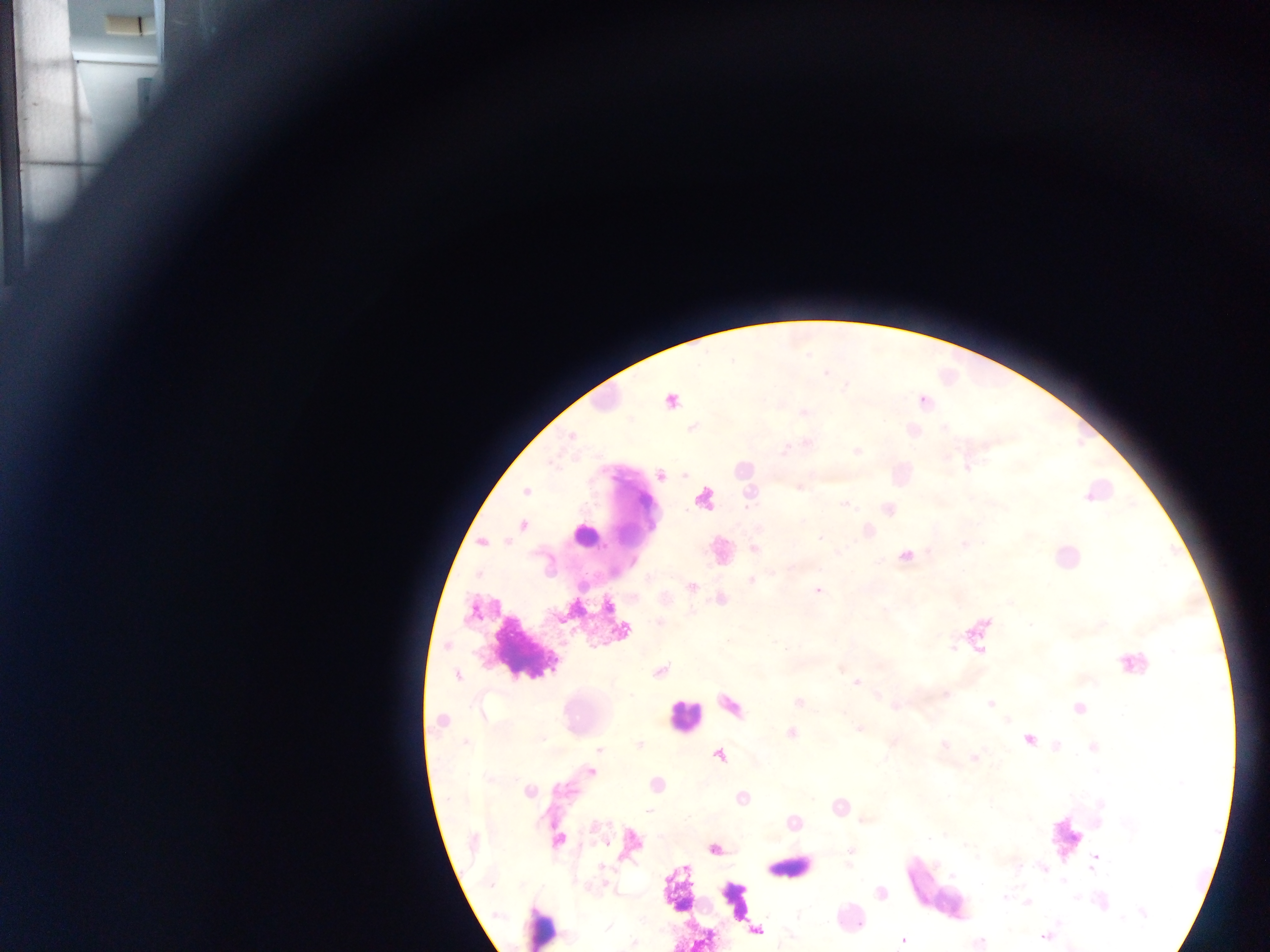 Approximate centers as {x, y} in pixels. Leukocyte locations: {584, 536}, {526, 649}, {1132, 663}, {684, 717}, {1067, 838}, {790, 868}, {676, 890}, {936, 890}, {736, 900}, {540, 926}. Malaria parasite locations: {670, 400}, {922, 401}, {912, 431}, {570, 436}, {856, 451}, {966, 466}, {660, 475}, {798, 485}, {525, 491}, {703, 499}, {844, 503}, {887, 508}, {522, 525}, {482, 542}, {963, 544}, {752, 549}, {905, 556}, {750, 581}, {691, 586}, {818, 590}, {720, 598}, {661, 623}, {621, 630}, {659, 671}, {457, 675}, {856, 682}, {944, 694}, {798, 702}, {990, 704}, {895, 705}, {730, 706}, {1077, 707}, {442, 721}, {860, 727}, {791, 732}, {1027, 739}, {639, 745}, {1093, 748}, {598, 749}, {718, 755}, {973, 757}, {591, 771}, {656, 784}, {528, 791}, {742, 797}, {838, 806}, {863, 819}, {791, 822}, {556, 839}, {631, 843}, {714, 849}, {851, 851}, {1094, 861}, {1042, 867}, {880, 892}, {1027, 901}, {756, 930}, {1046, 935}, {902, 939}, {633, 942}. Thick blood smear. Photographed through a microscope with a mobile-phone camera. Single field of view. Image is 1270×952 pixels. Collected in Ghana.